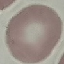
Summary:
  - Result: no malaria parasites detected
  - Image type: cell patch, automatically extracted from a larger field of view and resized to 64 × 64 pixels
  - Stain: Giemsa
  - Capture: smartphone through the microscope eyepiece
  - Preparation: thin blood smear